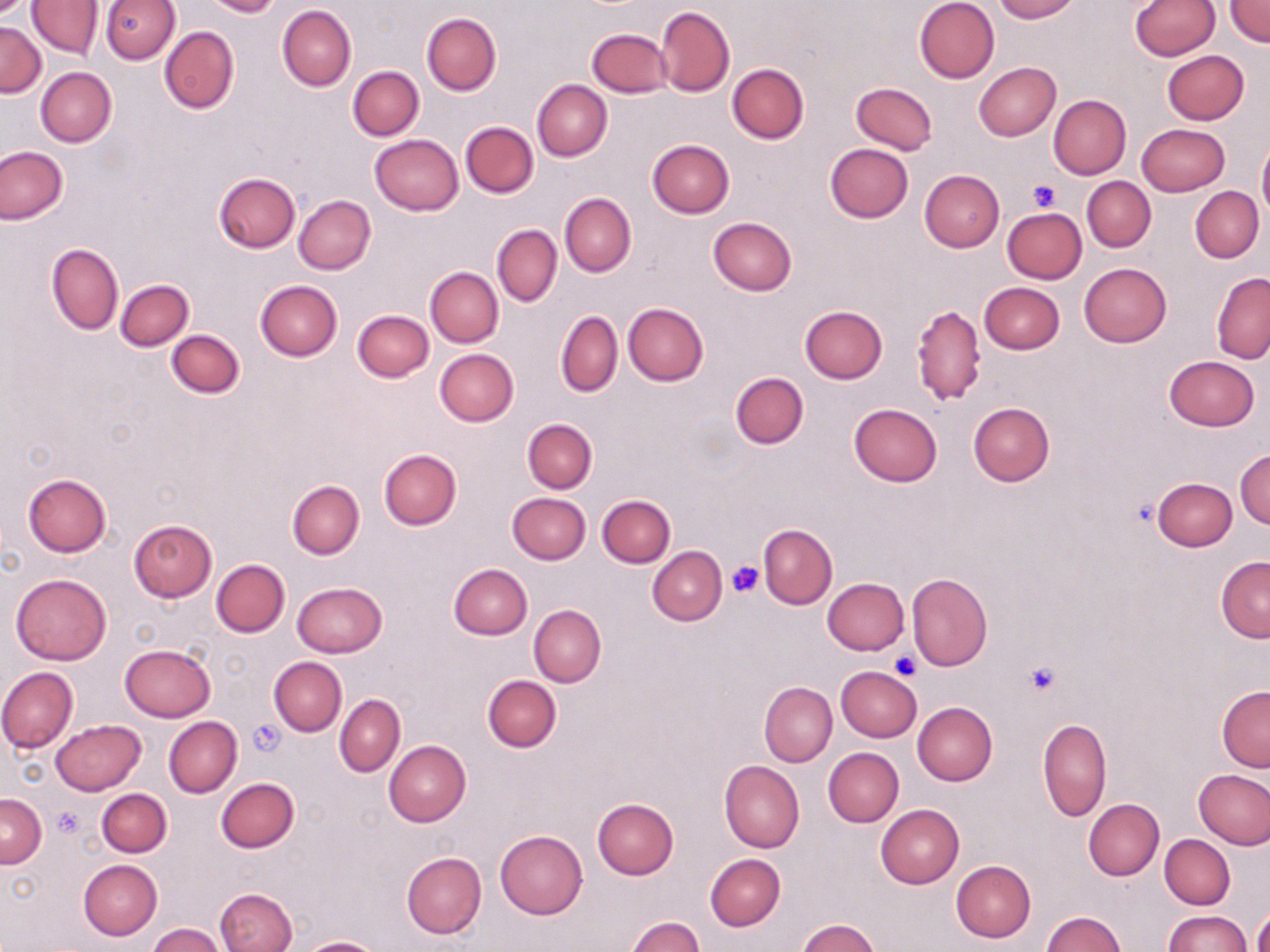

Approximate bounding boxes as named x1/y1/x2/y2 corners in pixels. Platelet locations: (x1=1027, y1=178, x2=1062, y2=210), (x1=728, y1=562, x2=764, y2=597), (x1=890, y1=651, x2=921, y2=679), (x1=1024, y1=661, x2=1061, y2=697), (x1=248, y1=720, x2=286, y2=755), (x1=53, y1=806, x2=84, y2=837). Uninfected red blood cell locations: (x1=99, y1=0, x2=180, y2=64), (x1=203, y1=0, x2=283, y2=18), (x1=914, y1=0, x2=1000, y2=83), (x1=993, y1=0, x2=1078, y2=22), (x1=27, y1=1, x2=103, y2=59), (x1=1129, y1=1, x2=1220, y2=59), (x1=1225, y1=1, x2=1270, y2=46), (x1=277, y1=5, x2=356, y2=91), (x1=654, y1=6, x2=734, y2=97), (x1=421, y1=13, x2=500, y2=95), (x1=0, y1=20, x2=45, y2=97), (x1=160, y1=26, x2=240, y2=113), (x1=587, y1=28, x2=672, y2=97), (x1=1162, y1=51, x2=1249, y2=125), (x1=974, y1=62, x2=1061, y2=140), (x1=726, y1=63, x2=809, y2=144), (x1=347, y1=66, x2=423, y2=141), (x1=35, y1=67, x2=116, y2=147), (x1=532, y1=80, x2=611, y2=161), (x1=851, y1=82, x2=936, y2=154), (x1=1048, y1=94, x2=1131, y2=178), (x1=460, y1=121, x2=538, y2=199), (x1=1136, y1=123, x2=1229, y2=197), (x1=370, y1=135, x2=462, y2=215), (x1=646, y1=139, x2=735, y2=218), (x1=1257, y1=139, x2=1270, y2=220), (x1=824, y1=144, x2=913, y2=223), (x1=0, y1=146, x2=68, y2=224), (x1=920, y1=170, x2=1004, y2=251), (x1=214, y1=173, x2=300, y2=252), (x1=1082, y1=176, x2=1156, y2=252), (x1=1190, y1=187, x2=1264, y2=263), (x1=560, y1=193, x2=636, y2=276), (x1=294, y1=195, x2=376, y2=274), (x1=1002, y1=208, x2=1086, y2=283), (x1=994, y1=209, x2=1075, y2=353), (x1=706, y1=217, x2=796, y2=297), (x1=492, y1=225, x2=562, y2=306), (x1=47, y1=243, x2=123, y2=336), (x1=1078, y1=263, x2=1171, y2=347), (x1=426, y1=267, x2=503, y2=347), (x1=1211, y1=272, x2=1270, y2=364), (x1=115, y1=279, x2=193, y2=350), (x1=255, y1=280, x2=342, y2=360), (x1=978, y1=282, x2=1064, y2=355), (x1=623, y1=303, x2=708, y2=386), (x1=911, y1=304, x2=985, y2=405), (x1=800, y1=306, x2=888, y2=384), (x1=353, y1=309, x2=433, y2=381), (x1=556, y1=311, x2=623, y2=397), (x1=167, y1=329, x2=244, y2=398), (x1=434, y1=348, x2=519, y2=426), (x1=1165, y1=355, x2=1259, y2=430), (x1=730, y1=371, x2=808, y2=448), (x1=968, y1=402, x2=1055, y2=485), (x1=848, y1=403, x2=942, y2=487), (x1=522, y1=418, x2=597, y2=493), (x1=515, y1=420, x2=591, y2=562), (x1=379, y1=447, x2=462, y2=529), (x1=1235, y1=448, x2=1269, y2=528), (x1=23, y1=473, x2=111, y2=556), (x1=1153, y1=477, x2=1236, y2=550), (x1=288, y1=479, x2=365, y2=559), (x1=507, y1=493, x2=590, y2=564), (x1=597, y1=494, x2=675, y2=568), (x1=128, y1=519, x2=216, y2=601), (x1=758, y1=524, x2=837, y2=608), (x1=647, y1=545, x2=726, y2=625), (x1=1215, y1=556, x2=1270, y2=643), (x1=211, y1=560, x2=289, y2=637), (x1=449, y1=563, x2=533, y2=639), (x1=10, y1=573, x2=111, y2=664), (x1=907, y1=573, x2=992, y2=671), (x1=822, y1=577, x2=909, y2=654), (x1=291, y1=582, x2=386, y2=658), (x1=529, y1=605, x2=606, y2=687), (x1=119, y1=644, x2=216, y2=722), (x1=269, y1=656, x2=347, y2=735), (x1=835, y1=666, x2=921, y2=742), (x1=0, y1=667, x2=78, y2=753), (x1=482, y1=674, x2=561, y2=753), (x1=757, y1=677, x2=916, y2=761), (x1=759, y1=682, x2=837, y2=766), (x1=1216, y1=685, x2=1269, y2=771), (x1=335, y1=694, x2=405, y2=776), (x1=913, y1=701, x2=997, y2=785), (x1=163, y1=716, x2=241, y2=798), (x1=1037, y1=718, x2=1111, y2=822), (x1=51, y1=720, x2=145, y2=795), (x1=383, y1=741, x2=471, y2=826), (x1=822, y1=747, x2=904, y2=827), (x1=719, y1=760, x2=805, y2=851), (x1=1194, y1=770, x2=1270, y2=849), (x1=216, y1=778, x2=299, y2=852), (x1=98, y1=788, x2=170, y2=856), (x1=0, y1=793, x2=46, y2=868), (x1=593, y1=797, x2=678, y2=879), (x1=1083, y1=798, x2=1163, y2=880), (x1=875, y1=805, x2=964, y2=888), (x1=495, y1=830, x2=587, y2=918), (x1=1160, y1=834, x2=1235, y2=909), (x1=400, y1=851, x2=486, y2=938), (x1=704, y1=854, x2=784, y2=931), (x1=78, y1=859, x2=163, y2=940), (x1=951, y1=860, x2=1036, y2=942), (x1=216, y1=888, x2=297, y2=952), (x1=1248, y1=906, x2=1269, y2=952), (x1=1043, y1=911, x2=1125, y2=952), (x1=1164, y1=911, x2=1250, y2=952), (x1=626, y1=915, x2=705, y2=952), (x1=797, y1=918, x2=880, y2=952), (x1=148, y1=924, x2=228, y2=952), (x1=299, y1=936, x2=385, y2=952). Slide-level diagnosis: no evidence of blood parasites. Image is 1270×952 pixels. May-Grünwald-Giemsa stain. Thin blood film. Captured at 1000x magnification. Light microscopy. Single field of view.